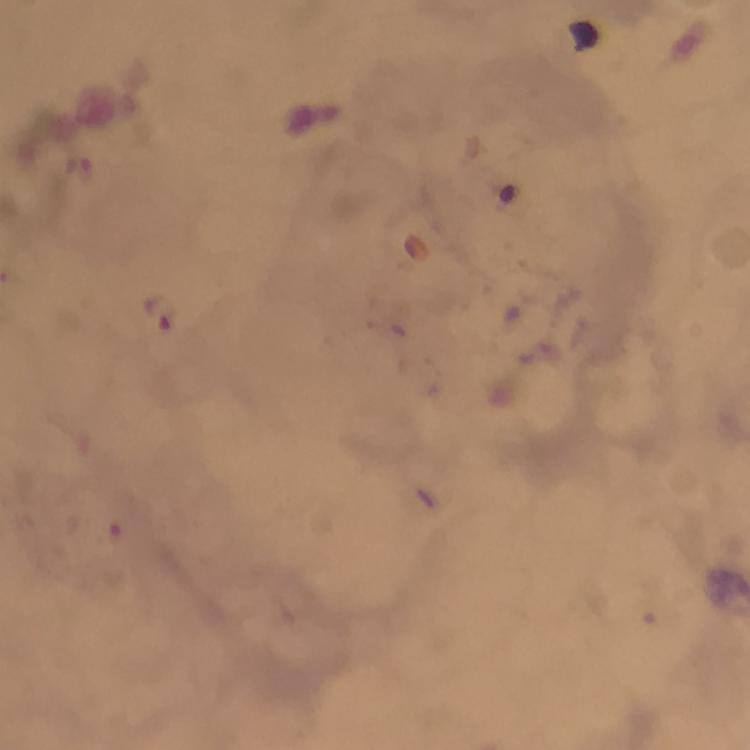
Approximate centers as [x, y] in pixels.
Summary:
  - Malaria parasite locations: [159, 312]
  - Preparation: thick blood smear
  - Image size: 750×750 pixels
  - Context: from a diagnostic examination for malaria
  - Capture: smartphone camera through the microscope
  - Magnification: 100x
  - Cropped from: a single field of view
  - Immersion oil: applied
  - Stain: Giemsa